Look for parasitized red blood cells.
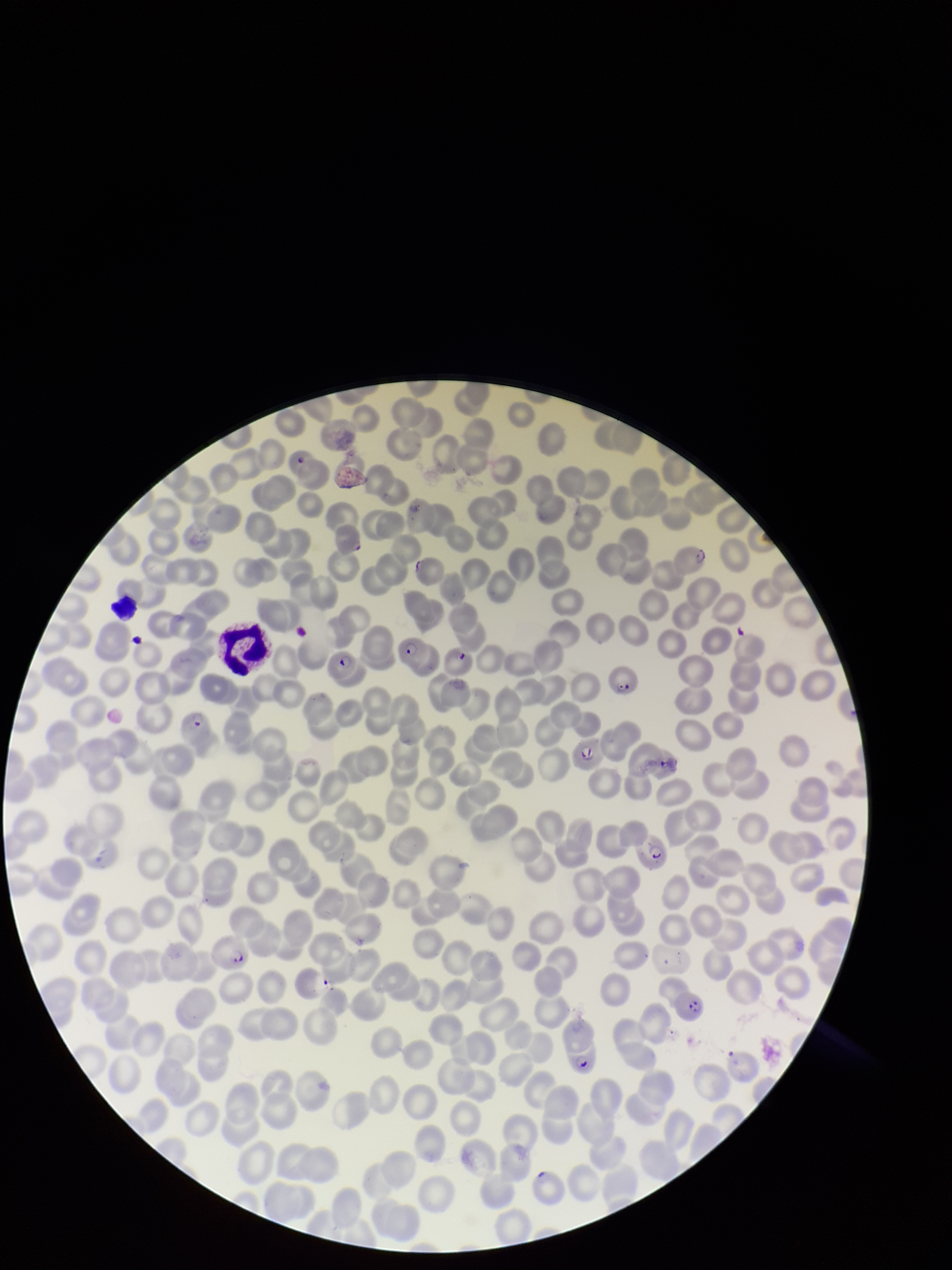
Identified.

{
  "preparation": "thin smear",
  "red_blood_cell_count": 219,
  "image_size": "952×1270 pixels",
  "stain": "Giemsa",
  "species_reported_for_this_patient": "Plasmodium falciparum",
  "parasitized_red_blood_cell_count": 15,
  "capture": "smartphone photograph through the microscope eyepiece",
  "field_of_view": "single",
  "patient_malaria_status": "infected"
}